State the blood parasite species.
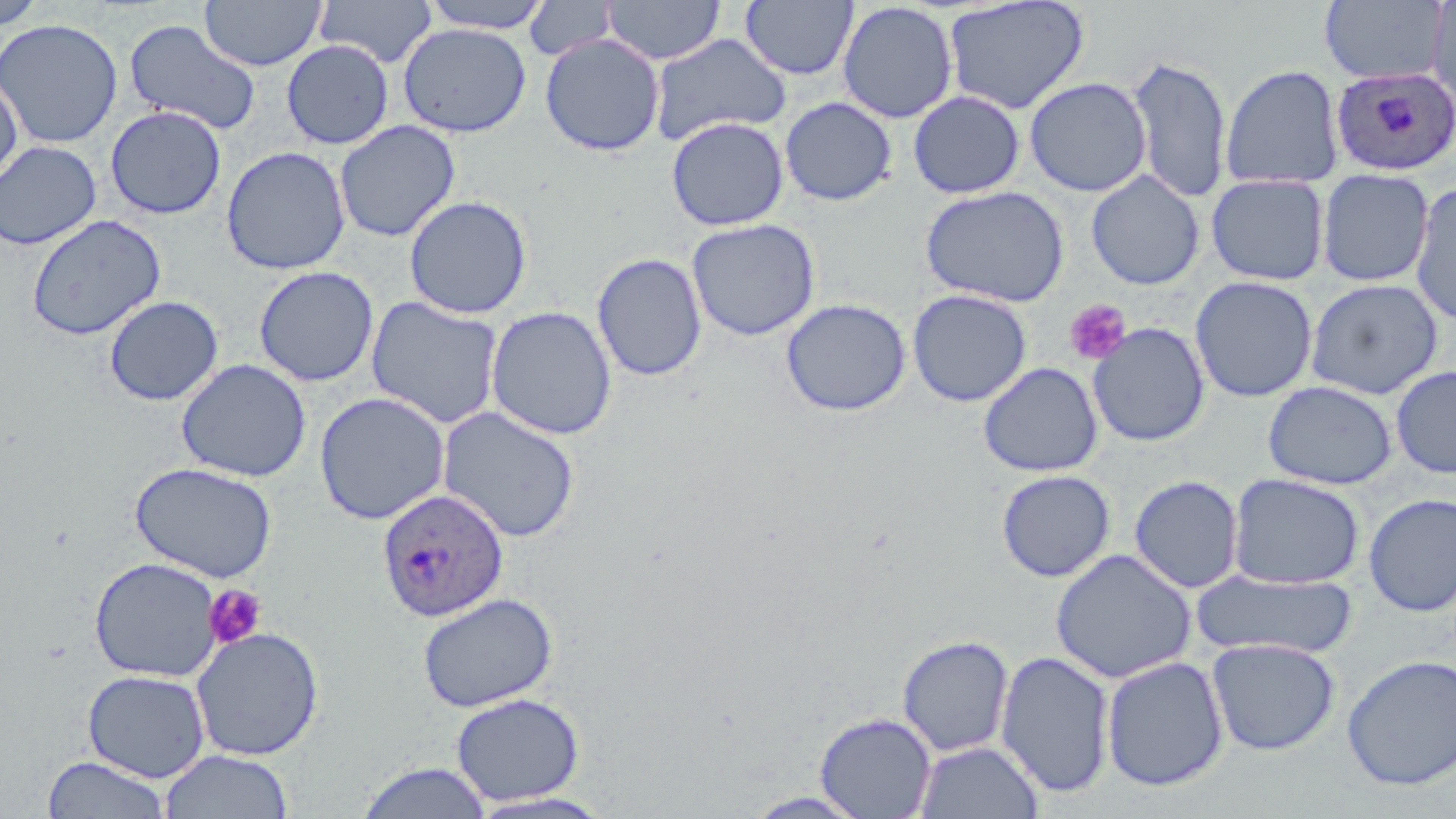
Plasmodium ovale.

Summary:
  - Coordinate format: approximate bounding boxes as named x1/y1/x2/y2 corners in pixels
  - Uninfected red blood cell locations: (x1=1, y1=0, x2=45, y2=29), (x1=200, y1=0, x2=326, y2=71), (x1=316, y1=0, x2=438, y2=68), (x1=419, y1=0, x2=554, y2=33), (x1=602, y1=0, x2=725, y2=65), (x1=943, y1=0, x2=1090, y2=114), (x1=1319, y1=0, x2=1449, y2=85), (x1=1428, y1=0, x2=1456, y2=117), (x1=524, y1=1, x2=618, y2=62), (x1=741, y1=1, x2=858, y2=81), (x1=837, y1=2, x2=958, y2=124), (x1=0, y1=18, x2=123, y2=149), (x1=124, y1=19, x2=261, y2=136), (x1=398, y1=23, x2=531, y2=138), (x1=648, y1=33, x2=791, y2=145), (x1=540, y1=34, x2=665, y2=156), (x1=281, y1=40, x2=394, y2=150), (x1=1128, y1=54, x2=1232, y2=204), (x1=1220, y1=64, x2=1345, y2=190), (x1=0, y1=75, x2=23, y2=186), (x1=1025, y1=77, x2=1151, y2=196), (x1=908, y1=90, x2=1025, y2=198), (x1=780, y1=96, x2=897, y2=206), (x1=105, y1=105, x2=227, y2=219), (x1=666, y1=117, x2=789, y2=230), (x1=335, y1=120, x2=460, y2=242), (x1=0, y1=140, x2=102, y2=250), (x1=221, y1=146, x2=350, y2=275), (x1=1317, y1=168, x2=1434, y2=287), (x1=1086, y1=171, x2=1204, y2=290), (x1=1206, y1=174, x2=1329, y2=286), (x1=1410, y1=181, x2=1456, y2=326), (x1=920, y1=185, x2=1070, y2=307), (x1=404, y1=195, x2=532, y2=319), (x1=26, y1=214, x2=166, y2=341), (x1=686, y1=218, x2=820, y2=341), (x1=592, y1=252, x2=707, y2=382), (x1=253, y1=266, x2=379, y2=387), (x1=1190, y1=276, x2=1317, y2=403), (x1=1306, y1=278, x2=1443, y2=399), (x1=907, y1=289, x2=1032, y2=407), (x1=103, y1=295, x2=223, y2=406), (x1=366, y1=296, x2=504, y2=430), (x1=781, y1=298, x2=911, y2=416), (x1=486, y1=305, x2=617, y2=440), (x1=1087, y1=322, x2=1210, y2=447), (x1=176, y1=358, x2=311, y2=482), (x1=979, y1=361, x2=1103, y2=477), (x1=1391, y1=365, x2=1456, y2=479), (x1=1263, y1=380, x2=1397, y2=489), (x1=314, y1=392, x2=450, y2=525), (x1=437, y1=406, x2=580, y2=543), (x1=129, y1=461, x2=279, y2=582), (x1=996, y1=469, x2=1115, y2=582), (x1=1228, y1=473, x2=1364, y2=590), (x1=1129, y1=475, x2=1244, y2=593), (x1=1363, y1=493, x2=1456, y2=617), (x1=1050, y1=549, x2=1197, y2=683), (x1=89, y1=557, x2=223, y2=682), (x1=1193, y1=570, x2=1358, y2=660), (x1=417, y1=592, x2=558, y2=712), (x1=190, y1=626, x2=325, y2=761), (x1=897, y1=635, x2=1014, y2=757), (x1=1206, y1=637, x2=1341, y2=756), (x1=996, y1=650, x2=1115, y2=798), (x1=1342, y1=654, x2=1456, y2=791), (x1=1101, y1=656, x2=1229, y2=792), (x1=83, y1=669, x2=210, y2=782), (x1=451, y1=692, x2=585, y2=806), (x1=815, y1=711, x2=937, y2=818), (x1=914, y1=740, x2=1044, y2=819), (x1=159, y1=749, x2=293, y2=818), (x1=42, y1=755, x2=170, y2=818), (x1=356, y1=761, x2=493, y2=819), (x1=466, y1=791, x2=616, y2=818)
  - Plasmodium ovale-infected red blood cell locations: (x1=1329, y1=66, x2=1456, y2=177), (x1=376, y1=488, x2=510, y2=622)
  - Platelet locations: (x1=1064, y1=299, x2=1131, y2=365), (x1=203, y1=585, x2=267, y2=650)
  - Field of view: one of a larger specimen
  - Modality: optical microscopy
  - Preparation: thin blood smear
  - Image size: 1456×819 pixels
  - Stain: May-Grünwald-Giemsa
  - Magnification: 1000x